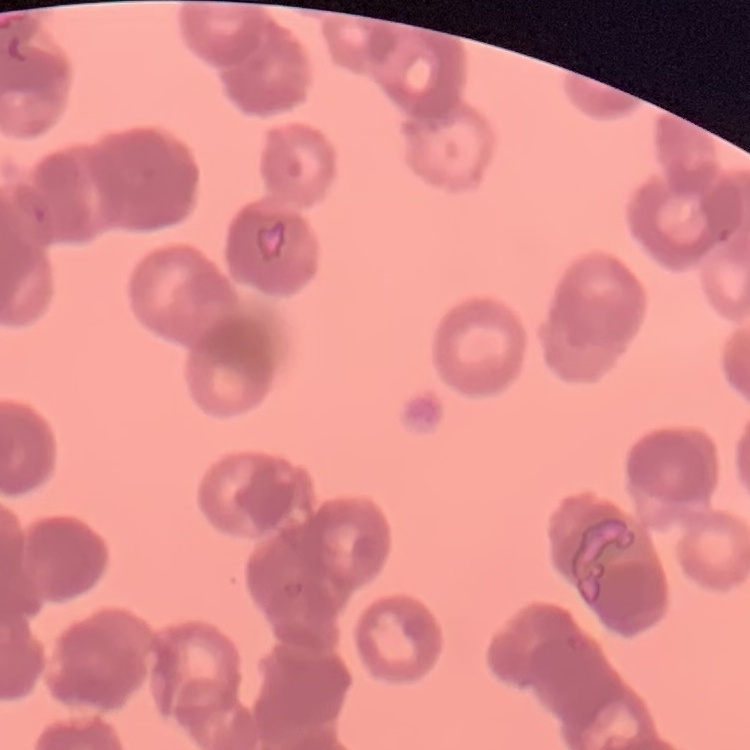 The red blood cells exhibit rouleaux formation. Thin blood film. Field's or Giemsa stain. Square crop of a larger photomicrograph.